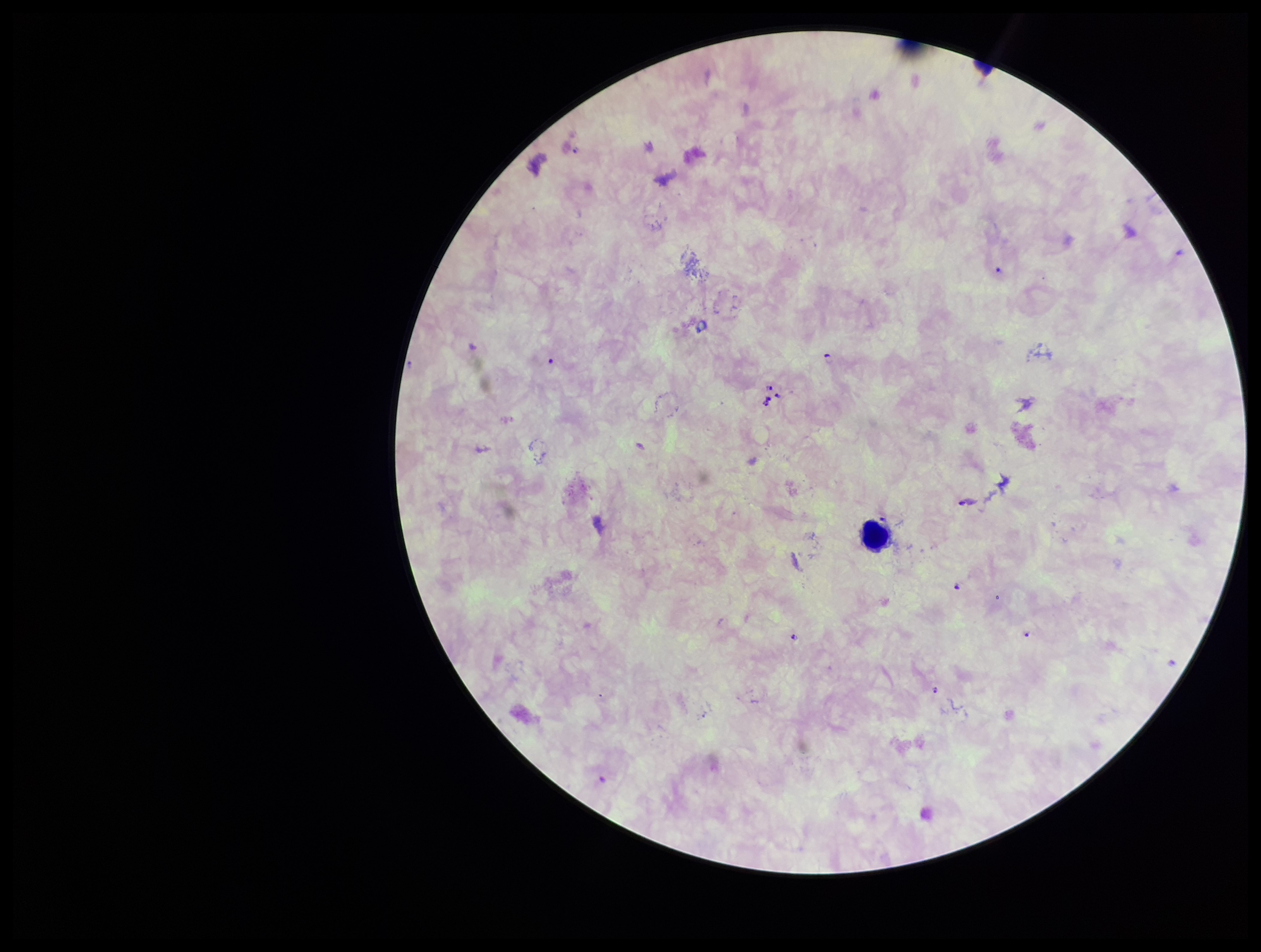
stain = Giemsa
capture = smartphone photograph through the microscope eyepiece
image size = 1261×952 pixels
field of view = single
parasite count = 10
preparation = thick blood smear
patient malaria status = positive
Plasmodium parasites = detected
species reported for this patient = Plasmodium falciparum
leukocyte count = 1